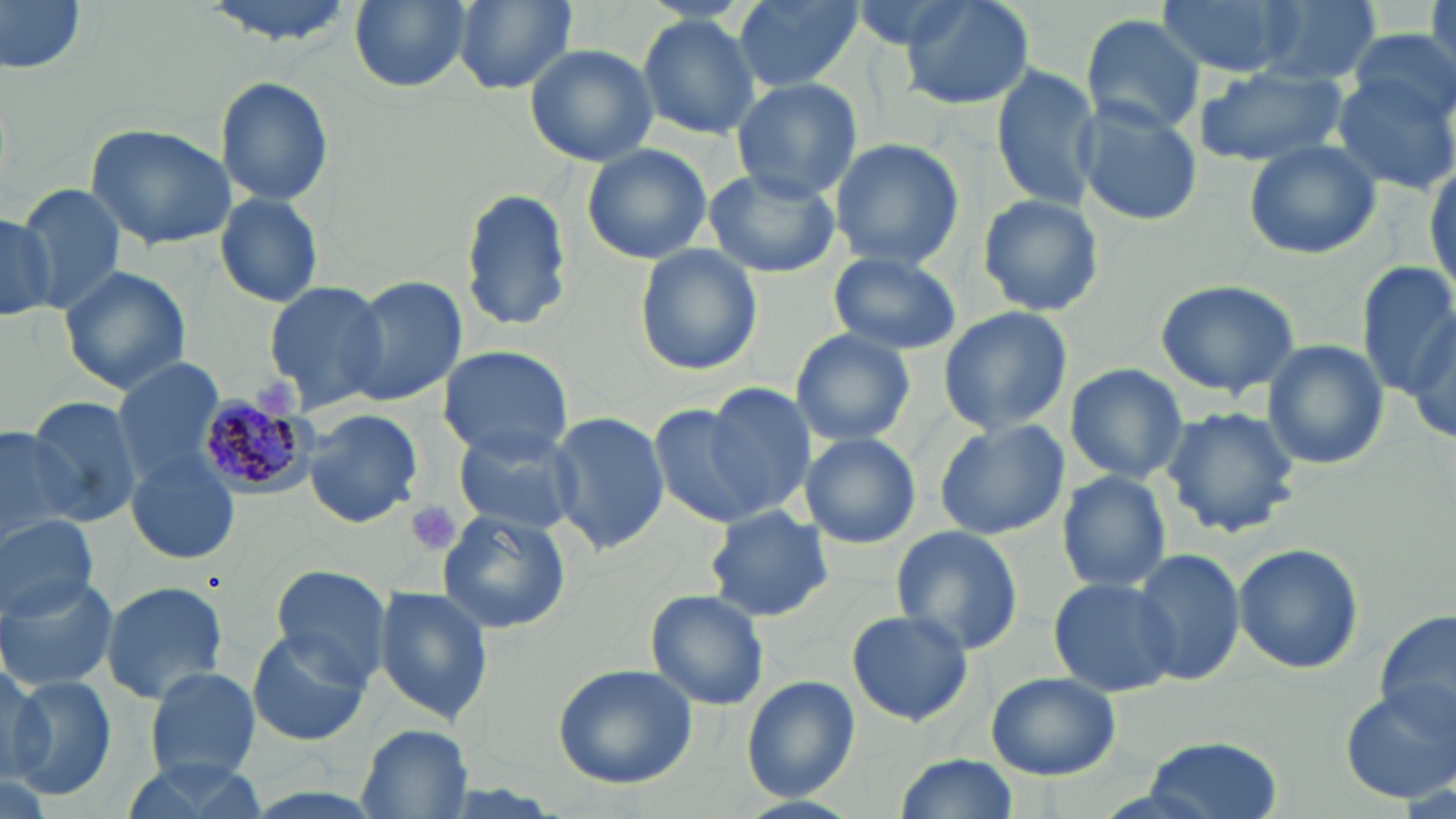

slide-level diagnosis = Plasmodium malariae
field of view = one of a larger specimen
magnification = 1000x
uninfected red blood cell locations = approximate bounding boxes as (x1, y1, x2, y2) in pixels: (1, 0, 86, 76), (196, 0, 360, 46), (350, 0, 469, 92), (451, 0, 580, 95), (732, 0, 865, 92), (839, 0, 972, 50), (897, 0, 1035, 111), (1159, 0, 1298, 78), (1256, 0, 1384, 85), (1428, 0, 1456, 81), (636, 13, 762, 139), (1080, 13, 1207, 136), (1347, 25, 1455, 123), (524, 43, 658, 168), (1192, 63, 1351, 168), (990, 64, 1098, 213), (1332, 71, 1456, 195), (216, 75, 334, 208), (729, 77, 863, 202), (1073, 102, 1203, 225), (84, 123, 238, 249), (830, 137, 964, 271), (1243, 139, 1381, 261), (581, 143, 712, 264), (1426, 161, 1456, 298), (703, 164, 844, 278), (13, 182, 129, 314), (459, 185, 574, 335), (213, 192, 326, 309), (977, 193, 1103, 320), (0, 214, 57, 321), (636, 247, 762, 374), (829, 252, 961, 355), (1356, 263, 1454, 402), (58, 265, 191, 394), (341, 275, 467, 407), (1154, 277, 1303, 397), (261, 278, 391, 410), (938, 306, 1072, 434), (1405, 313, 1456, 448), (790, 329, 915, 446), (1262, 339, 1390, 470), (434, 345, 575, 462), (110, 359, 225, 485), (1063, 362, 1189, 484), (699, 384, 817, 518), (26, 397, 145, 526), (647, 399, 768, 527), (1160, 406, 1303, 540), (302, 408, 422, 528), (549, 412, 667, 555), (933, 420, 1068, 539), (0, 423, 82, 545), (450, 423, 585, 538), (801, 433, 921, 549), (125, 454, 237, 566), (1057, 471, 1173, 594), (703, 505, 836, 623), (437, 510, 571, 635), (0, 516, 98, 622), (888, 525, 1024, 656), (1234, 542, 1364, 674), (1129, 548, 1245, 687), (268, 563, 396, 689), (1047, 576, 1179, 698), (0, 577, 120, 693), (100, 580, 229, 705), (373, 586, 493, 725), (646, 589, 770, 712), (845, 609, 974, 727), (1375, 609, 1453, 737), (247, 627, 372, 746), (0, 654, 49, 784), (553, 662, 699, 789), (145, 666, 261, 782), (986, 671, 1120, 780), (5, 675, 117, 799), (740, 676, 863, 805), (1337, 684, 1455, 804), (357, 726, 474, 818), (1141, 734, 1281, 817), (898, 752, 1017, 819), (119, 754, 269, 817)
Plasmodium malariae-infected red blood cell locations = approximate bounding boxes as (x1, y1, x2, y2) in pixels: (197, 392, 320, 498)
preparation = thin blood smear
modality = optical microscopy
stain = May-Grünwald-Giemsa
image size = 1456×819 pixels
platelet locations = approximate bounding boxes as (x1, y1, x2, y2) in pixels: (253, 374, 299, 420), (407, 500, 461, 558)